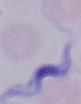

identification = trypanosome
magnification = 1000x
modality = micrograph